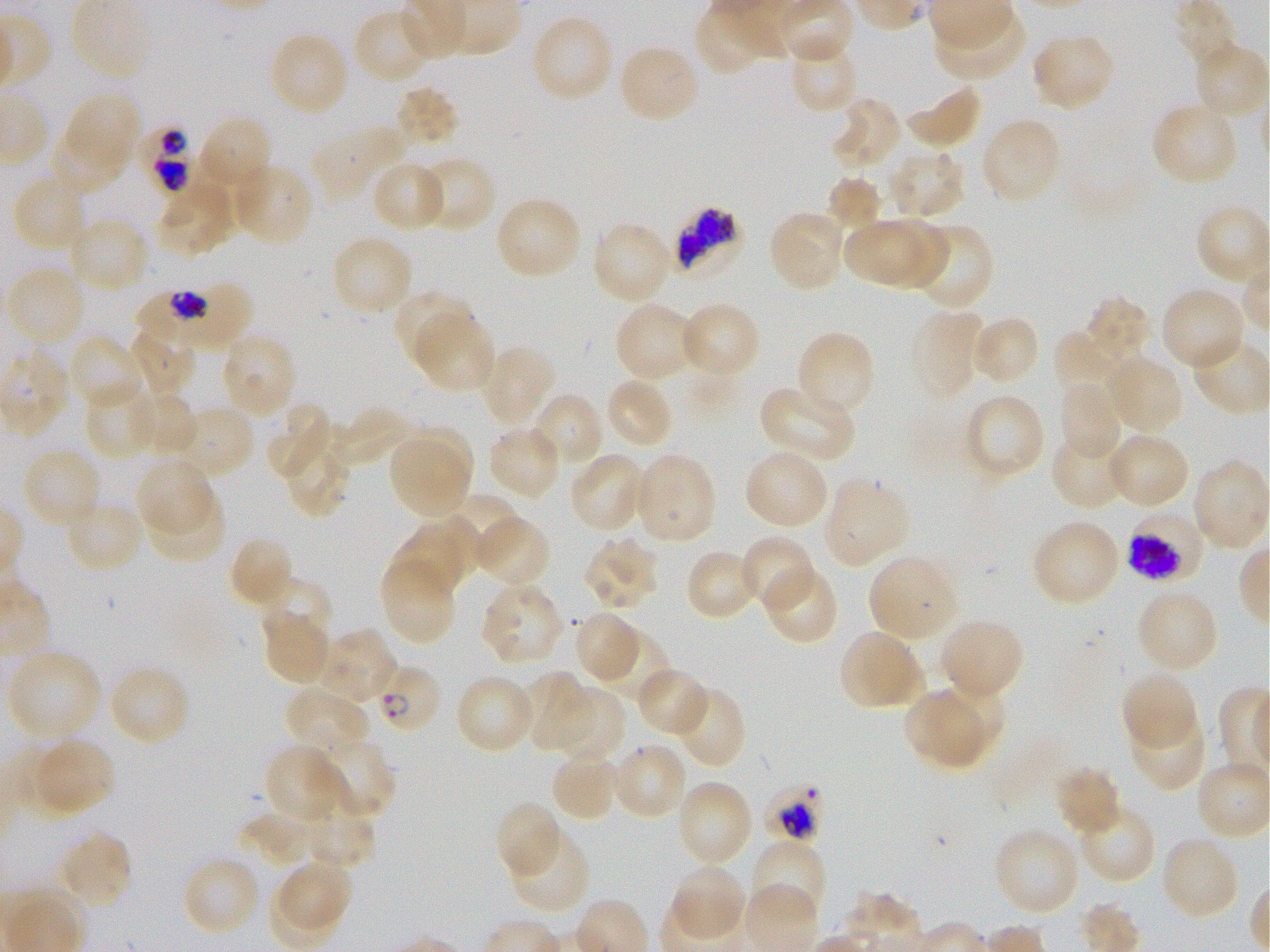
Not every red blood cell is marked. A life-cycle stage — or a range of stages, where the recorded stages span more than one — follows each staged infected red blood cell.
{
  "stain": "Giemsa",
  "locations_of_infected_red_blood_cells": "approximate bounding boxes as {x1, y1, x2, y2} in pixels: {135, 119, 196, 199}; {677, 208, 741, 274}; {136, 287, 208, 357} early trophozoite; {1124, 508, 1205, 585} schizont; {365, 662, 441, 736} ring; {756, 778, 827, 841}",
  "donor_blood_group": "O+",
  "image_size": "1270×952 pixels",
  "objective": "100x, oil immersion, numerical aperture 1.25",
  "field_of_view": "one from this slide",
  "preparation": "thin blood smear",
  "life_cycle_stages_observed": "ring, trophozoite, schizont",
  "locations_of_uninfected_red_blood_cells": "approximate bounding boxes as {x1, y1, x2, y2} in pixels: {1174, 0, 1239, 70}, {932, 7, 1027, 82}, {353, 8, 437, 85}, {529, 14, 614, 103}, {268, 30, 350, 117}, {1030, 30, 1116, 111}, {788, 34, 860, 114}, {1194, 42, 1270, 120}, {616, 43, 702, 125}, {904, 81, 983, 150}, {394, 85, 460, 154}, {57, 92, 140, 186}, {831, 96, 904, 172}, {1150, 100, 1239, 187}, {195, 114, 273, 200}, {979, 116, 1062, 206}, {311, 124, 406, 202}, {885, 146, 966, 220}, {415, 156, 497, 233}, {370, 160, 449, 232}, {231, 162, 314, 248}, {12, 171, 91, 253}, {826, 176, 881, 233}, {156, 179, 237, 258}, {494, 195, 583, 281}, {1194, 203, 1270, 286}, {768, 209, 849, 293}, {885, 216, 951, 290}, {66, 217, 149, 293}, {840, 217, 920, 285}, {590, 220, 673, 306}, {919, 225, 994, 312}, {330, 235, 414, 318}, {4, 265, 88, 347}, {194, 284, 254, 341}, {1160, 285, 1246, 372}, {393, 289, 475, 367}, {1085, 297, 1151, 360}, {614, 302, 700, 383}, {678, 302, 762, 381}, {911, 309, 986, 401}, {413, 311, 497, 395}, {969, 314, 1040, 386}, {1056, 323, 1122, 397}, {129, 325, 199, 398}, {794, 329, 876, 418}, {219, 333, 298, 420}, {66, 334, 145, 413}, {0, 336, 74, 440}, {478, 343, 555, 430}, {1104, 354, 1184, 435}, {604, 376, 675, 450}, {1056, 380, 1123, 461}, {83, 381, 155, 460}, {758, 385, 856, 465}, {126, 388, 198, 458}, {530, 391, 605, 473}, {963, 392, 1047, 480}, {263, 404, 334, 483}, {168, 405, 256, 482}, {331, 406, 415, 468}, {398, 424, 477, 496}, {279, 425, 352, 520}, {486, 425, 562, 500}, {1050, 432, 1129, 510}, {1104, 432, 1190, 511}, {391, 442, 467, 515}, {21, 447, 102, 529}, {744, 448, 830, 530}, {630, 451, 717, 546}, {567, 452, 648, 534}, {134, 456, 217, 539}, {1190, 458, 1270, 552}, {821, 476, 910, 569}, {148, 494, 231, 569}, {443, 494, 523, 568}, {64, 500, 146, 574}, {471, 516, 551, 590}, {1030, 518, 1123, 607}, {391, 528, 465, 599}, {583, 534, 662, 612}, {739, 534, 818, 614}, {228, 535, 295, 609}, {685, 548, 761, 620}, {868, 553, 960, 645}, {380, 554, 459, 645}, {761, 563, 839, 645}, {259, 579, 332, 644}, {479, 579, 566, 666}, {1135, 587, 1220, 675}, {261, 607, 333, 688}, {571, 610, 644, 685}, {940, 618, 1024, 698}, {589, 626, 671, 705}, {315, 627, 398, 705}, {839, 629, 925, 711}, {5, 648, 102, 743}, {107, 664, 192, 747}, {633, 667, 710, 737}, {1120, 671, 1199, 753}, {518, 672, 593, 753}, {454, 674, 537, 756}, {286, 684, 371, 757}, {933, 685, 1006, 751}, {551, 686, 627, 764}, {671, 686, 746, 770}, {902, 693, 984, 765}, {1126, 708, 1207, 792}, {27, 737, 116, 817}, {317, 738, 394, 813}, {611, 741, 688, 822}, {263, 744, 337, 821}, {550, 748, 624, 822}, {1053, 765, 1123, 836}, {674, 779, 754, 868}, {493, 800, 563, 880}, {304, 802, 377, 868}, {1076, 803, 1157, 884}, {245, 807, 313, 863}, {992, 826, 1081, 917}, {507, 827, 590, 916}, {56, 830, 133, 911}, {1160, 834, 1241, 922}, {749, 837, 827, 925}, {181, 855, 262, 937}, {278, 858, 354, 931}, {668, 864, 747, 944}",
  "culture": "P. falciparum strain 3D7, static, in vitro"
}